Identify the parasite.
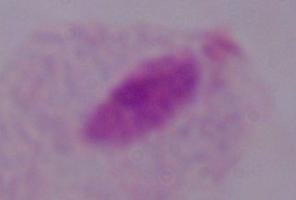
This is a trichomonad.

Captured at 1000x magnification. Micrograph.